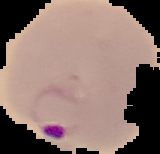

result = Plasmodium parasites identified
image size = 160×154 pixels
image type = cell region segmented out of the field of view; surrounding area masked to black
preparation = thin blood smear